Outline each blood parasite and name the species.
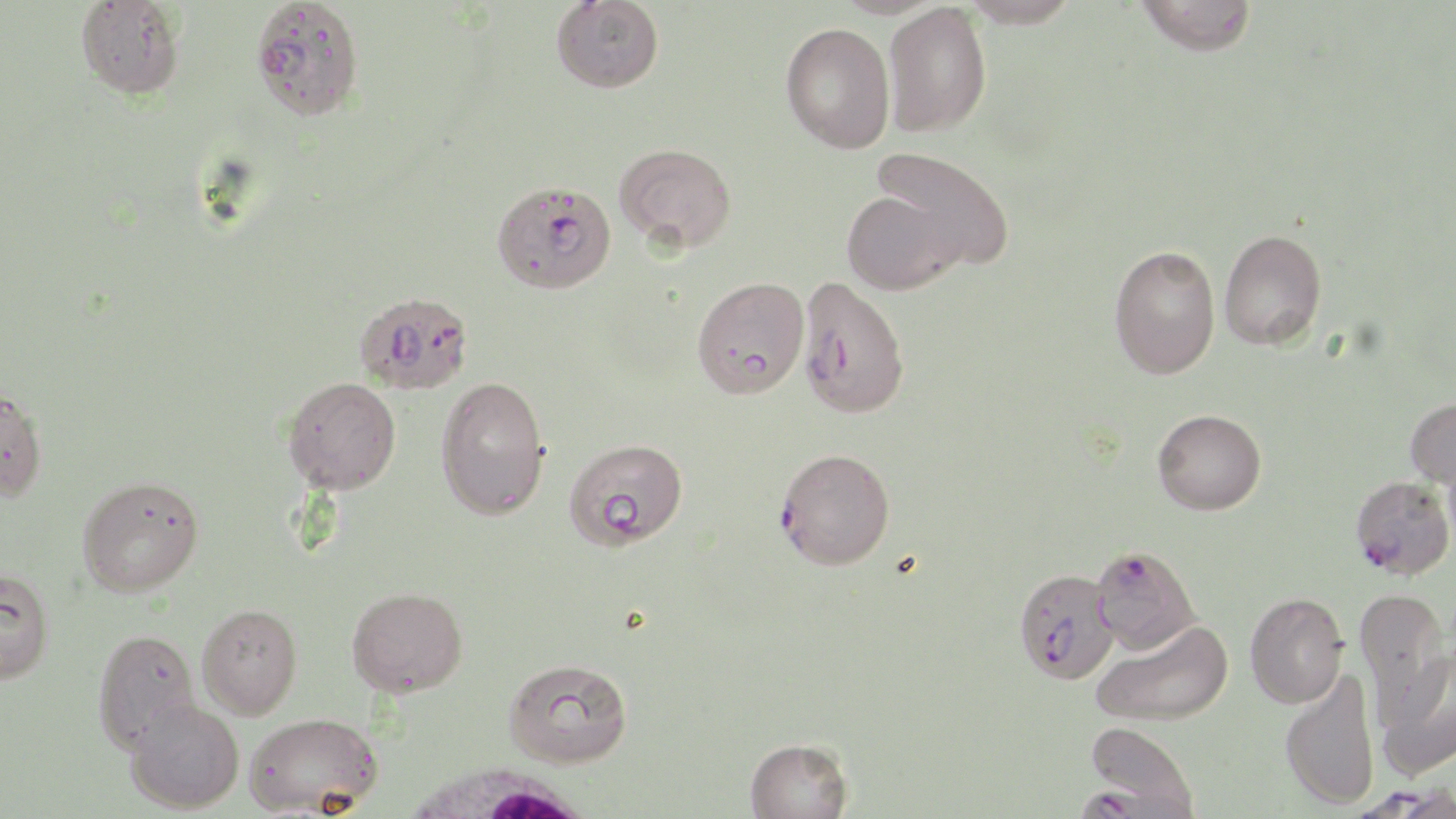

Approximate bounding boxes as (x1, y1, x2, y2) in pixels.
Plasmodium falciparum-infected red blood cells: (250, 0, 365, 121), (491, 180, 617, 294), (796, 275, 910, 418), (353, 290, 474, 395), (776, 446, 895, 570), (1350, 474, 1454, 579), (1090, 544, 1201, 654), (1013, 567, 1119, 683), (1076, 787, 1189, 819).
No Plasmodium ovale, Plasmodium malariae, Plasmodium vivax, Babesia divergens, or Trypanosoma brucei observed.

Uninfected red blood cell locations: (75, 0, 186, 100), (551, 0, 664, 93), (960, 0, 1080, 28), (1135, 0, 1258, 56), (882, 3, 992, 137), (780, 22, 895, 154), (614, 141, 736, 252), (869, 146, 1015, 272), (841, 190, 964, 294), (1219, 228, 1327, 351), (1109, 244, 1220, 380), (691, 276, 809, 398), (436, 375, 550, 520), (282, 376, 401, 494), (0, 384, 48, 502), (1405, 396, 1456, 490), (1152, 409, 1266, 515), (564, 437, 689, 550), (77, 475, 204, 597), (0, 566, 54, 684), (346, 586, 468, 697), (1354, 586, 1450, 722), (1244, 592, 1349, 708), (197, 603, 303, 718), (1091, 619, 1232, 728), (92, 627, 200, 753), (1373, 653, 1455, 783), (504, 658, 633, 768), (1279, 668, 1380, 809), (125, 697, 244, 813), (245, 711, 383, 816), (1085, 721, 1200, 816), (745, 736, 853, 819). White blood cell locations: (398, 762, 602, 819). Slide-level diagnosis: Plasmodium falciparum. Image is 1456×819 pixels. May-Grünwald-Giemsa stain. 1000x magnification. Optical microscopy. Single field of view. Thin blood smear.